Report the malaria status.
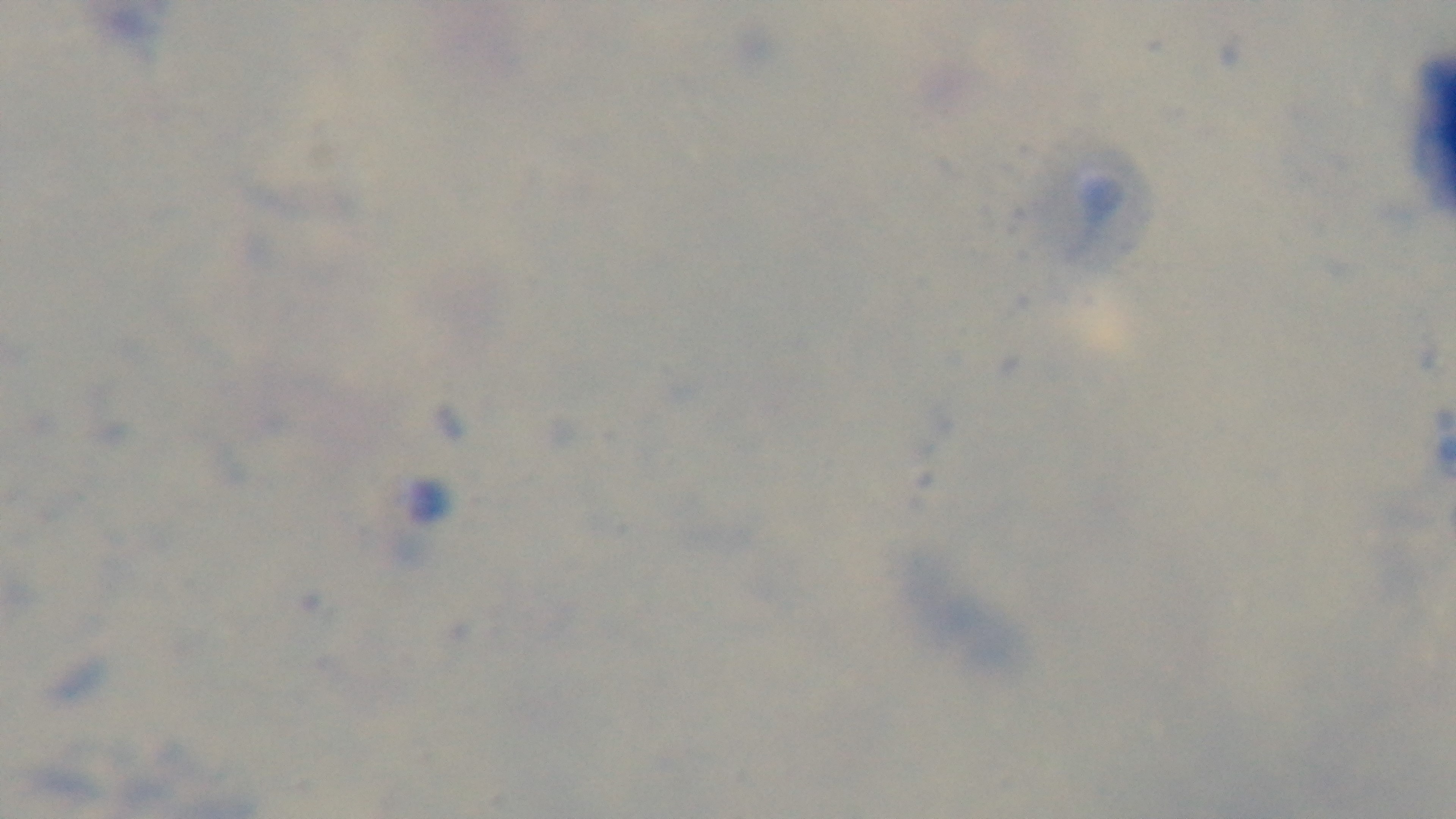

It is uninfected.

{
  "modality": "light microscopy",
  "field_of_view": "one from the slide",
  "objective": "100x oil immersion",
  "preparation": "thick",
  "stain": "Giemsa",
  "capture": "mounted 4K digital camera"
}